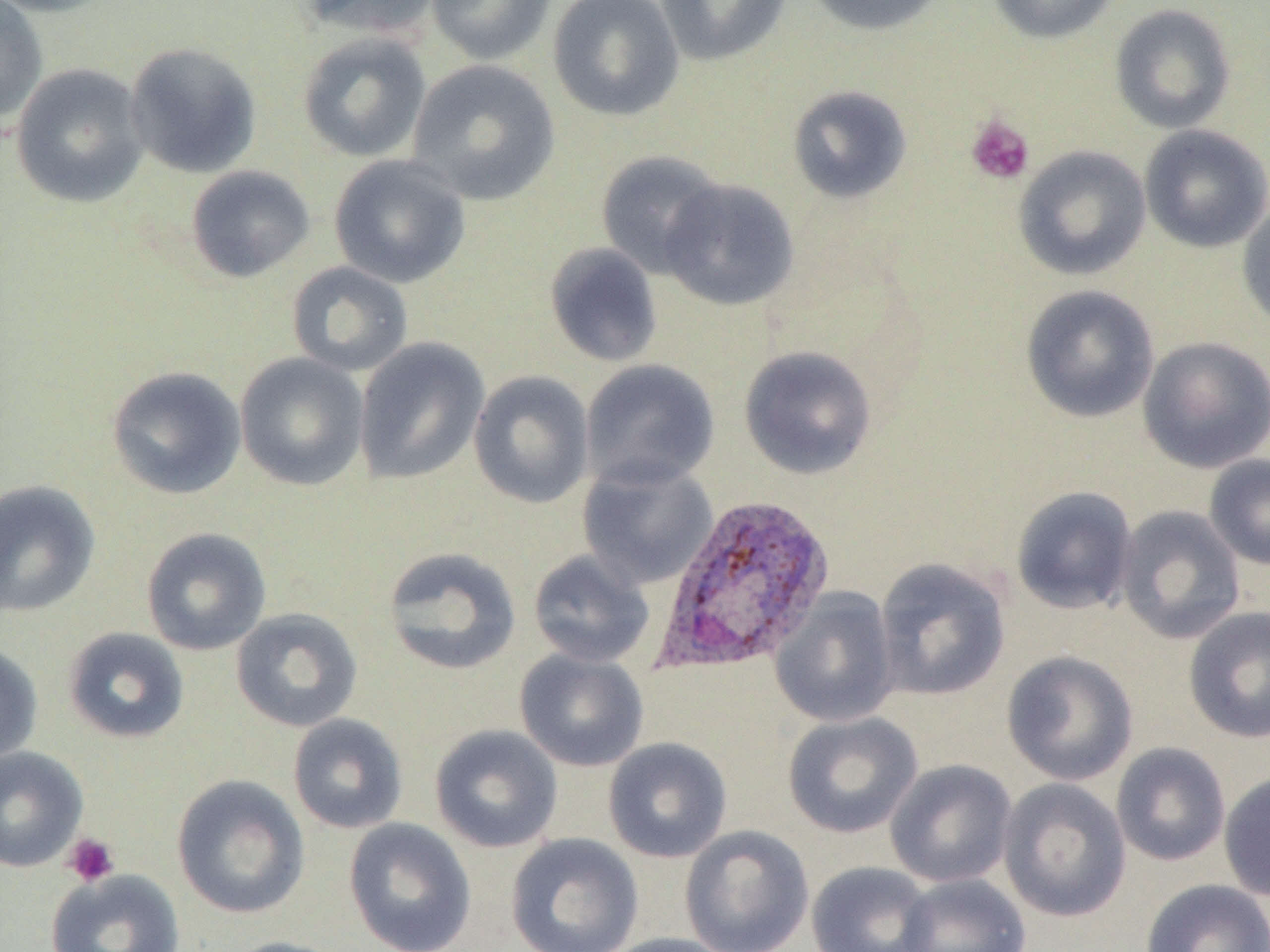

Summary:
  - Coordinate format: approximate bounding boxes as (x1,y1)-(x2,y2) corner pairs in pixels
  - Platelet locations: (965,114)-(1034,185), (62,832)-(120,887)
  - Plasmodium vivax-infected red blood cell locations: (652,491)-(836,675)
  - Uninfected red blood cell locations: (0,0)-(119,18), (0,0)-(48,127), (296,0)-(443,40), (426,0)-(557,65), (547,0)-(685,122), (654,0)-(792,67), (801,0)-(948,36), (987,0)-(1121,44), (1109,3)-(1237,134), (297,31)-(432,162), (124,42)-(262,178), (407,59)-(560,206), (10,63)-(150,208), (787,84)-(913,204), (1139,124)-(1270,253), (1013,145)-(1151,281), (595,149)-(727,278), (328,154)-(472,289), (185,165)-(315,283), (659,178)-(800,312), (1237,201)-(1270,334), (544,243)-(663,367), (286,262)-(414,378), (1020,284)-(1159,423), (1137,336)-(1270,473), (353,337)-(491,486), (739,346)-(877,479), (234,352)-(370,491), (579,359)-(720,491), (106,365)-(246,500), (468,370)-(594,509), (1204,454)-(1270,570), (576,460)-(718,590), (0,480)-(100,617), (1010,486)-(1139,616), (1115,505)-(1246,645), (140,526)-(272,656), (381,546)-(523,675), (527,549)-(655,668), (874,557)-(1010,701), (770,589)-(899,727), (1183,605)-(1270,743), (230,607)-(363,732), (62,626)-(190,744), (0,641)-(43,765), (514,649)-(649,772), (1001,650)-(1139,786), (782,712)-(923,839), (287,713)-(408,834), (429,724)-(564,853), (603,737)-(732,863), (1110,742)-(1231,866), (0,745)-(88,873), (884,758)-(1017,887), (1219,770)-(1270,902), (172,774)-(310,919), (998,778)-(1131,922), (343,817)-(477,952), (679,825)-(814,952), (505,832)-(644,952), (806,860)-(937,952), (46,868)-(186,952), (895,872)-(1031,952), (1140,878)-(1270,952), (598,933)-(735,952), (219,936)-(355,952)
  - Slide-level diagnosis: Plasmodium vivax
  - Field of view: single
  - Modality: optical microscopy
  - Preparation: thin blood smear
  - Image size: 1270×952 pixels
  - Magnification: 1000x